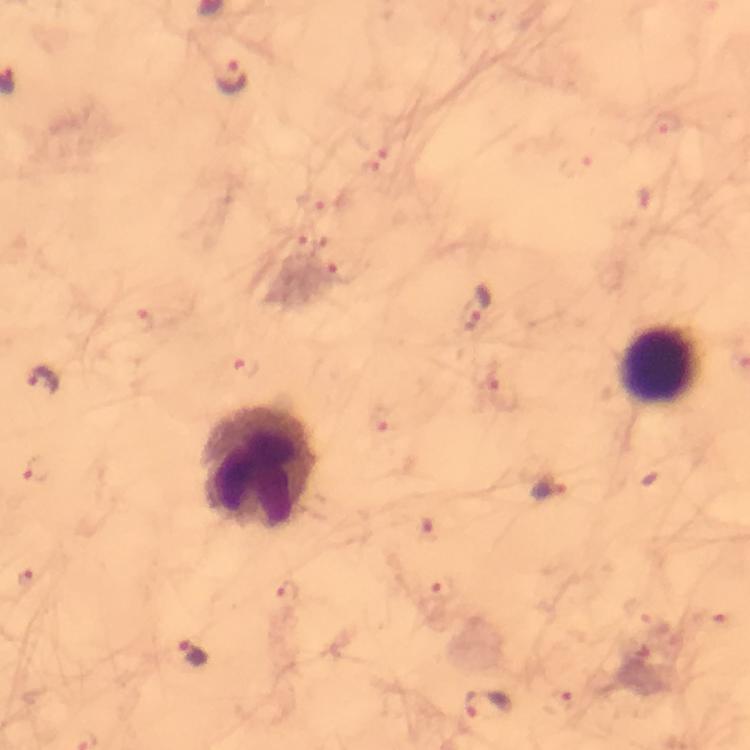
capture: smartphone mounted on the microscope
cropped_from: one field of view
image_size: 750×750 pixels
stain: Giemsa
leukocyte_locations: 'approximate centers as {x, y} in pixels: {659, 364}, {261, 467}'
immersion_oil: applied
magnification: 100x
malaria_parasite_locations: 'approximate centers as {x, y} in pixels: {231, 78}, {669, 123}, {576, 165}, {317, 203}, {300, 241}, {343, 272}, {475, 310}, {141, 320}, {250, 366}, {44, 381}, {505, 395}, {379, 416}, {34, 469}, {544, 487}, {26, 580}, {440, 592}, {288, 594}, {716, 620}, {194, 652}, {557, 702}, {488, 707}'
context: from a malaria diagnostic workup
preparation: thick smear